Locate every blood parasite and identify its species.
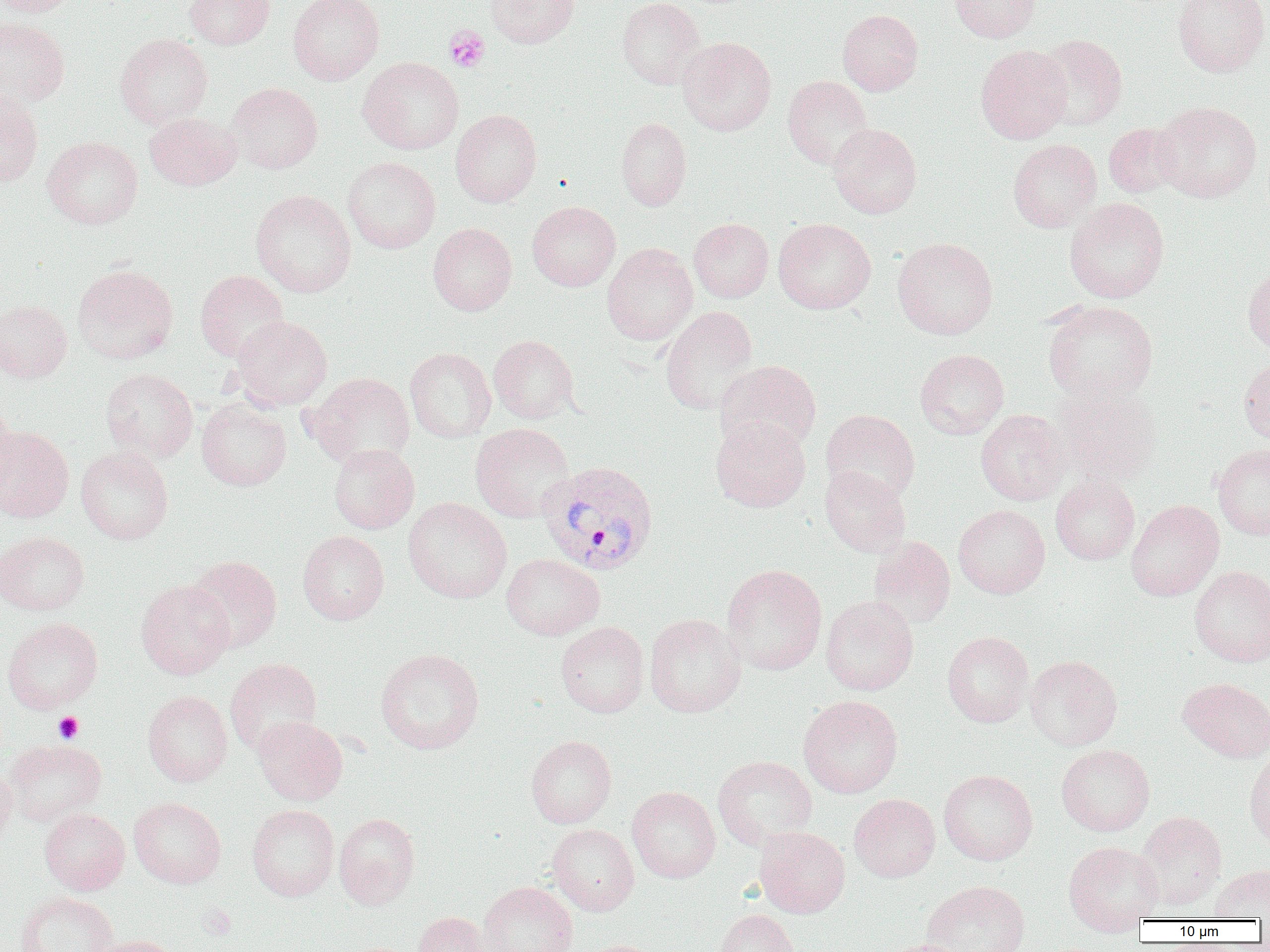

Approximate bounding boxes as (x1, y1, x2, y2) in pixels.
Plasmodium vivax-infected red blood cells: (537, 460, 659, 576).
No Plasmodium falciparum, Plasmodium ovale, Plasmodium malariae, Babesia divergens, or Trypanosoma brucei observed.

Summary:
  - Uninfected red blood cell locations: (0, 0, 80, 17), (183, 0, 275, 49), (288, 0, 384, 85), (486, 0, 579, 48), (617, 0, 706, 89), (949, 0, 1041, 43), (1172, 0, 1269, 78), (837, 9, 923, 96), (0, 17, 70, 107), (115, 34, 213, 128), (1036, 34, 1128, 131), (678, 37, 776, 136), (975, 44, 1073, 144), (358, 56, 464, 155), (782, 75, 873, 169), (226, 82, 323, 174), (0, 88, 44, 188), (1152, 101, 1262, 203), (450, 109, 542, 207), (144, 113, 241, 191), (616, 117, 692, 211), (828, 123, 922, 218), (1103, 123, 1183, 199), (42, 136, 143, 229), (1008, 138, 1102, 233), (342, 156, 441, 254), (250, 189, 357, 297), (1065, 197, 1169, 303), (527, 201, 621, 291), (689, 218, 773, 302), (774, 218, 876, 314), (428, 222, 517, 316), (892, 237, 997, 339), (602, 244, 698, 345), (72, 264, 178, 364), (1242, 266, 1270, 354), (195, 270, 289, 363), (0, 300, 72, 383), (1042, 300, 1158, 403), (660, 306, 759, 415), (229, 315, 333, 411), (489, 335, 579, 423), (405, 348, 496, 443), (915, 348, 1009, 439), (1239, 357, 1270, 445), (715, 359, 822, 454), (101, 368, 198, 462), (304, 372, 415, 469), (1052, 380, 1162, 486), (196, 398, 291, 491), (0, 402, 19, 504), (821, 409, 920, 503), (976, 410, 1069, 506), (711, 417, 811, 512), (470, 422, 574, 523), (0, 426, 74, 523), (1212, 443, 1270, 540), (328, 444, 419, 533), (76, 445, 174, 545), (819, 466, 911, 557), (1050, 475, 1139, 565), (403, 497, 512, 603), (1126, 499, 1224, 601), (953, 505, 1050, 598), (0, 531, 89, 615), (297, 531, 389, 624), (869, 536, 956, 628), (501, 553, 604, 640), (186, 555, 282, 652), (721, 564, 827, 675), (1189, 565, 1270, 667), (135, 579, 234, 679), (820, 595, 918, 696), (644, 614, 746, 717), (2, 617, 103, 713), (555, 622, 649, 717), (942, 631, 1034, 727), (375, 647, 485, 754), (1024, 655, 1122, 750), (224, 658, 322, 756), (1178, 677, 1270, 762), (143, 690, 233, 787), (798, 695, 903, 798), (253, 716, 347, 805), (525, 735, 616, 828), (4, 738, 107, 827), (1056, 744, 1155, 836), (1245, 748, 1270, 850), (713, 755, 817, 849), (0, 765, 17, 848), (939, 770, 1038, 865), (627, 786, 720, 883), (849, 793, 940, 882), (128, 796, 226, 888), (247, 804, 339, 901), (39, 808, 130, 895), (1136, 811, 1227, 909), (334, 812, 420, 908), (547, 824, 639, 916), (754, 826, 850, 918), (1063, 841, 1164, 932), (1209, 864, 1270, 921), (921, 880, 1030, 952), (478, 881, 578, 952), (15, 892, 119, 952), (715, 909, 800, 952), (413, 912, 490, 952), (88, 934, 183, 952), (877, 938, 976, 952), (575, 940, 663, 952)
  - Platelet locations: (444, 25, 490, 73), (53, 712, 83, 744), (197, 902, 236, 941)
  - Slide-level diagnosis: Plasmodium vivax
  - Field of view: one of a larger specimen
  - Preparation: thin blood smear
  - Magnification: 1000x
  - Image size: 1270×952 pixels
  - Modality: optical microscopy